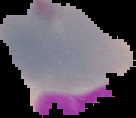
{
  "image_type": "segmented cell region on a black background",
  "preparation": "thin blood film",
  "image_size": "136×118 pixels",
  "malaria_status": "uninfected"
}